Assess the morphology of the red blood cells.
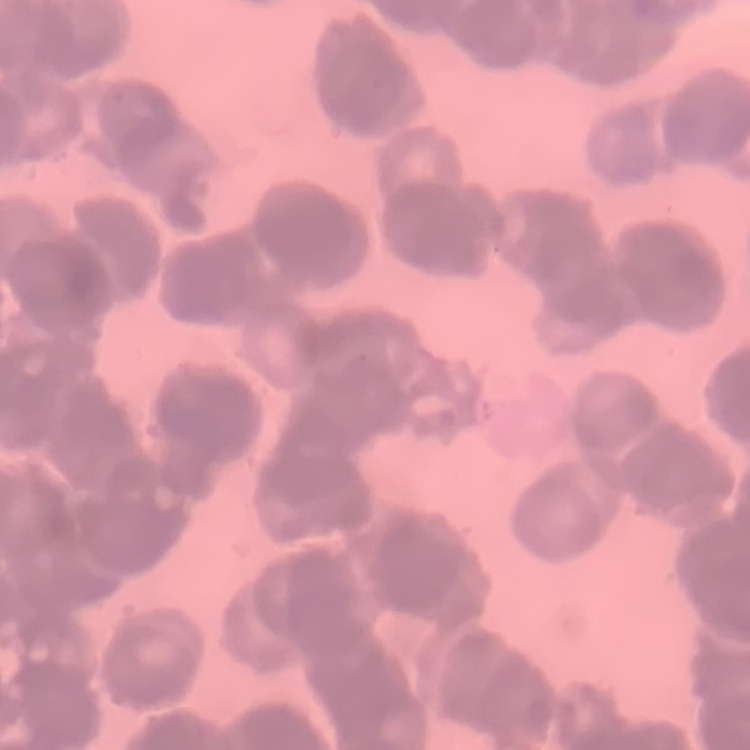
They show rouleaux formation.

Field's or Giemsa stain. Thin blood smear. Square crop of a larger photomicrograph.